Locate every blood parasite and identify its species.
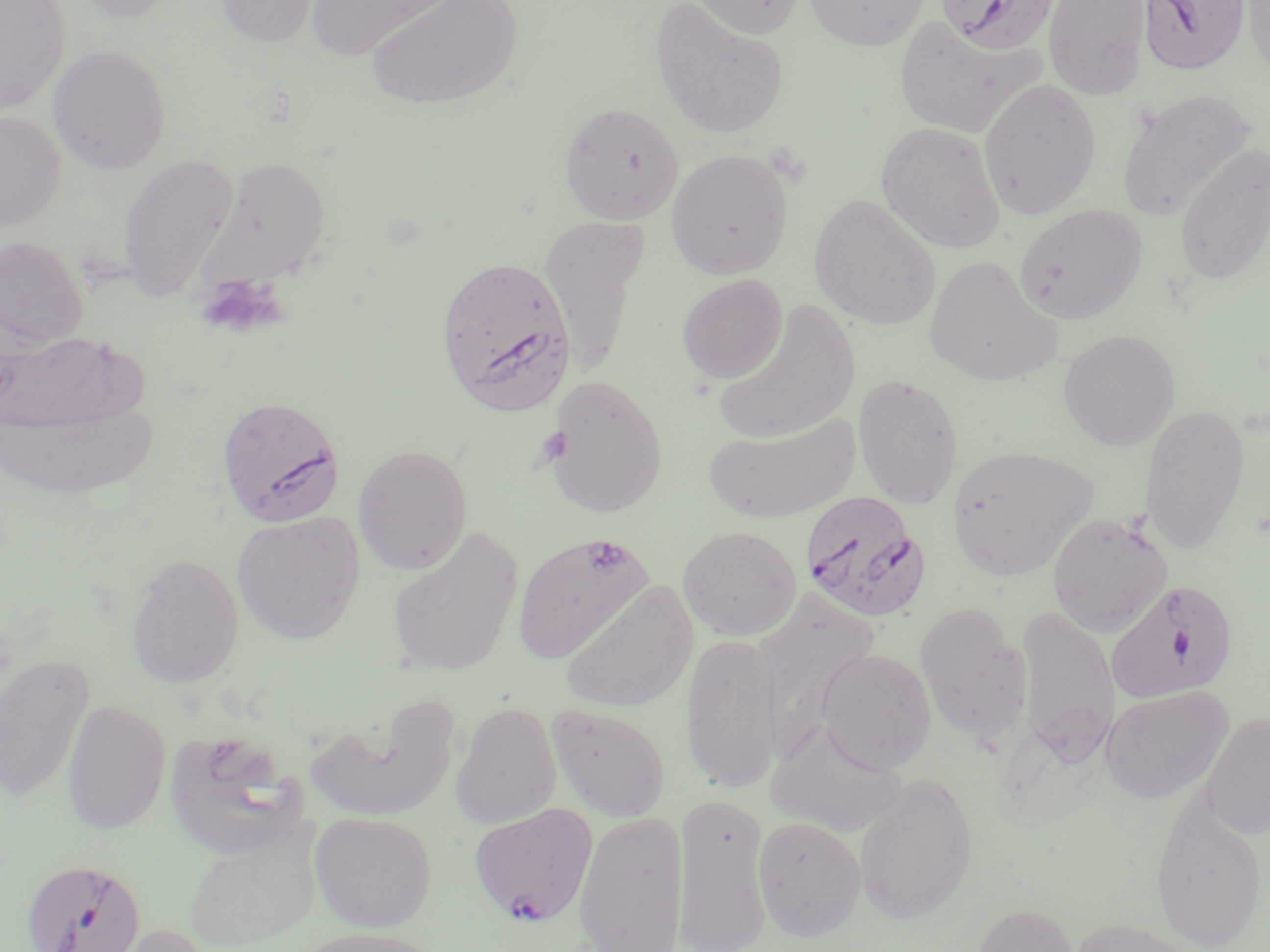
Approximate bounding boxes as (x1, y1, x2, y2) in pixels.
Plasmodium falciparum-infected red blood cells: (936, 0, 1058, 54), (1139, 0, 1250, 75), (436, 254, 576, 414), (215, 394, 346, 527), (799, 490, 930, 623), (1105, 578, 1239, 705), (469, 802, 599, 928), (20, 858, 147, 952).
No Plasmodium ovale, Plasmodium malariae, Plasmodium vivax, Babesia divergens, or Trypanosoma brucei observed.

Platelet locations: (196, 275, 284, 339), (581, 537, 631, 578). Uninfected red blood cell locations: (0, 0, 69, 114), (67, 0, 183, 22), (215, 0, 322, 47), (304, 0, 458, 62), (363, 0, 525, 111), (686, 0, 806, 39), (804, 0, 930, 50), (1043, 0, 1151, 100), (1242, 0, 1270, 80), (651, 1, 789, 139), (893, 15, 1040, 137), (48, 45, 171, 174), (978, 78, 1101, 220), (1116, 88, 1255, 221), (559, 101, 684, 224), (0, 110, 66, 231), (875, 121, 1006, 253), (1174, 142, 1270, 286), (666, 150, 793, 280), (117, 154, 239, 304), (194, 156, 332, 293), (809, 194, 941, 331), (1014, 204, 1147, 324), (540, 214, 649, 375), (1, 236, 88, 347), (924, 255, 1062, 387), (677, 273, 788, 385), (712, 301, 862, 446), (1058, 328, 1181, 450), (0, 329, 139, 436), (852, 373, 964, 508), (544, 374, 669, 519), (4, 397, 158, 501), (1140, 403, 1251, 555), (703, 411, 860, 524), (353, 443, 473, 576), (945, 444, 1100, 582), (231, 511, 364, 644), (1047, 512, 1173, 638), (387, 525, 524, 675), (678, 526, 802, 641), (512, 533, 654, 664), (126, 552, 244, 687), (560, 581, 697, 713), (914, 602, 1032, 745), (1014, 605, 1120, 764), (682, 632, 781, 794), (816, 648, 937, 773), (0, 653, 95, 804), (1101, 685, 1235, 804), (61, 698, 171, 835), (309, 700, 459, 823), (450, 702, 562, 828), (547, 703, 671, 822), (1201, 711, 1270, 839), (766, 718, 908, 838), (163, 729, 310, 859), (853, 772, 979, 926), (1149, 789, 1268, 952), (674, 795, 772, 952), (573, 810, 690, 952), (309, 811, 437, 932), (752, 815, 866, 941), (183, 823, 322, 950), (971, 904, 1079, 952), (1068, 916, 1203, 952), (102, 923, 220, 952), (296, 926, 444, 952). Slide-level diagnosis: Plasmodium falciparum. Light microscopy. May-Grünwald-Giemsa-stained preparation. Single field of view. 1000x magnification. Image is 1270×952 pixels. Thin blood smear.